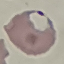
Summary:
  - Malaria status: parasitized
  - Capture: smartphone camera at the microscope eyepiece
  - Image type: automatically extracted cell patch, resized to 64 × 64 pixels
  - Preparation: thin blood film
  - Stain: Giemsa